Identify the preparation type.
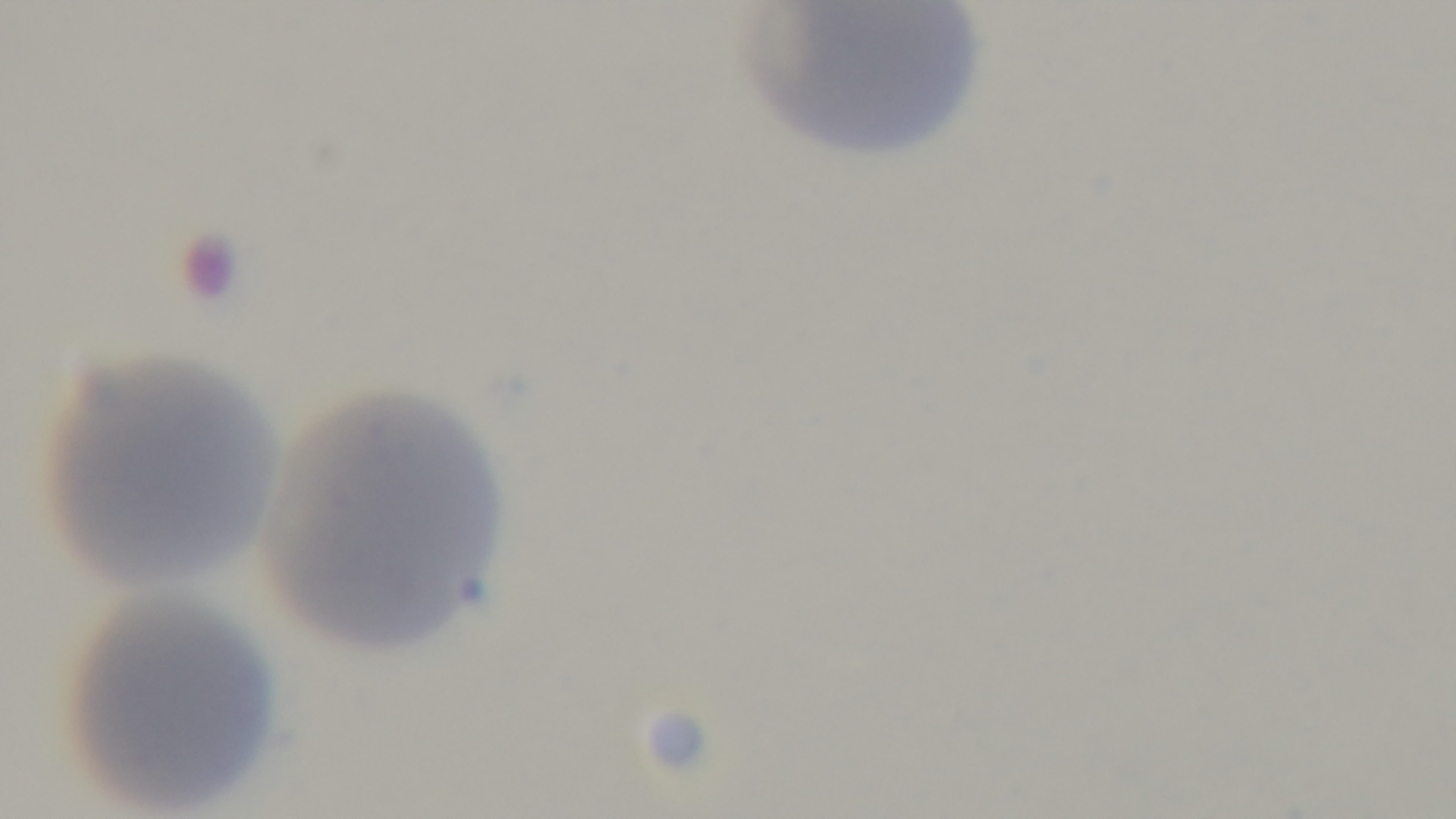
A thin smear.

Summary:
  - Modality: light microscopy
  - Malaria status: uninfected
  - Stain: Giemsa
  - Capture: mounted 4K digital camera
  - Field of view: one from the slide
  - Objective: 100x oil immersion